Give the position of every malaria parasite.
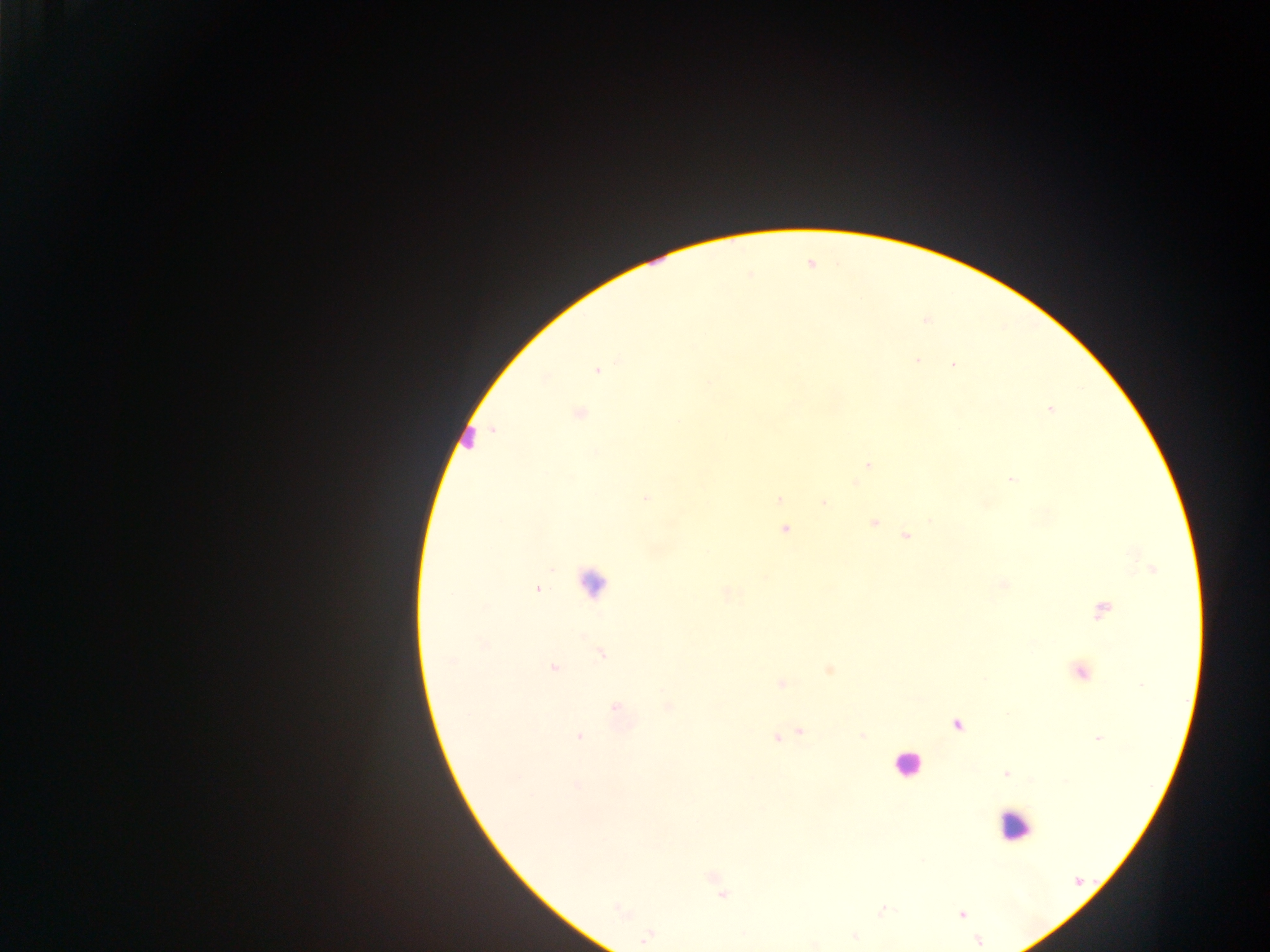

Approximate centers as [x, y] in pixels.
Malaria parasites: [917, 359], [952, 365], [597, 370], [1050, 409], [580, 413], [869, 465], [1010, 479], [855, 483], [646, 498], [779, 500], [824, 503], [873, 523], [784, 529], [906, 536], [1004, 584], [538, 589], [1102, 611], [601, 654], [554, 668], [829, 670], [1080, 673], [781, 684], [669, 706], [615, 708], [956, 724], [800, 732], [862, 735], [579, 736], [776, 738], [1097, 738], [1006, 774], [577, 784], [722, 895], [619, 909], [961, 914], [854, 936], [646, 937], [979, 941].

Leukocyte locations: [465, 438], [591, 583], [905, 764], [1013, 825]. Mobile-phone photograph taken through the microscope. Sample from Ghana. One field of view. Image is 1270×952 pixels. Thick blood smear.